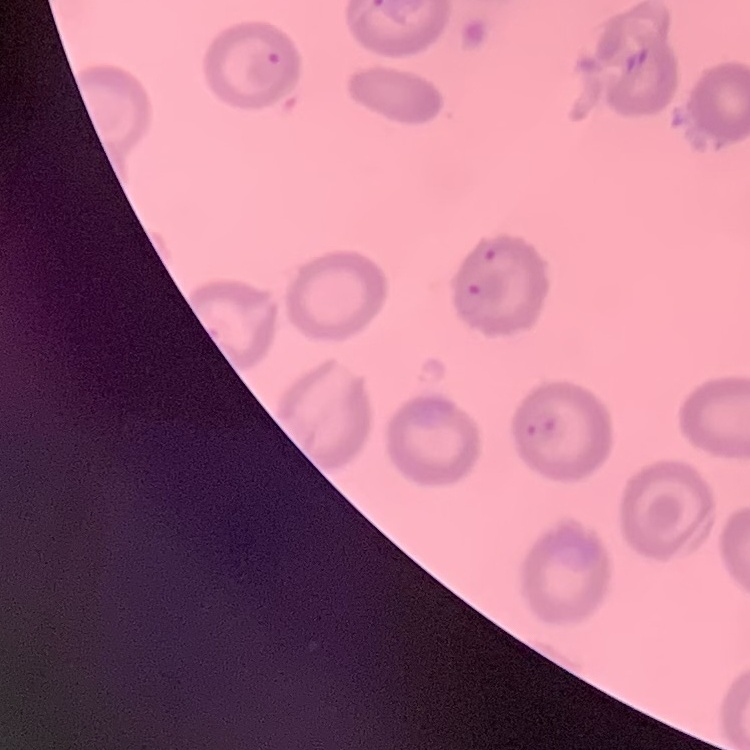

The red blood cells show no rouleaux formation. Thin blood smear. Stained with either Field's or Giemsa. One tile cut from a larger photomicrograph.